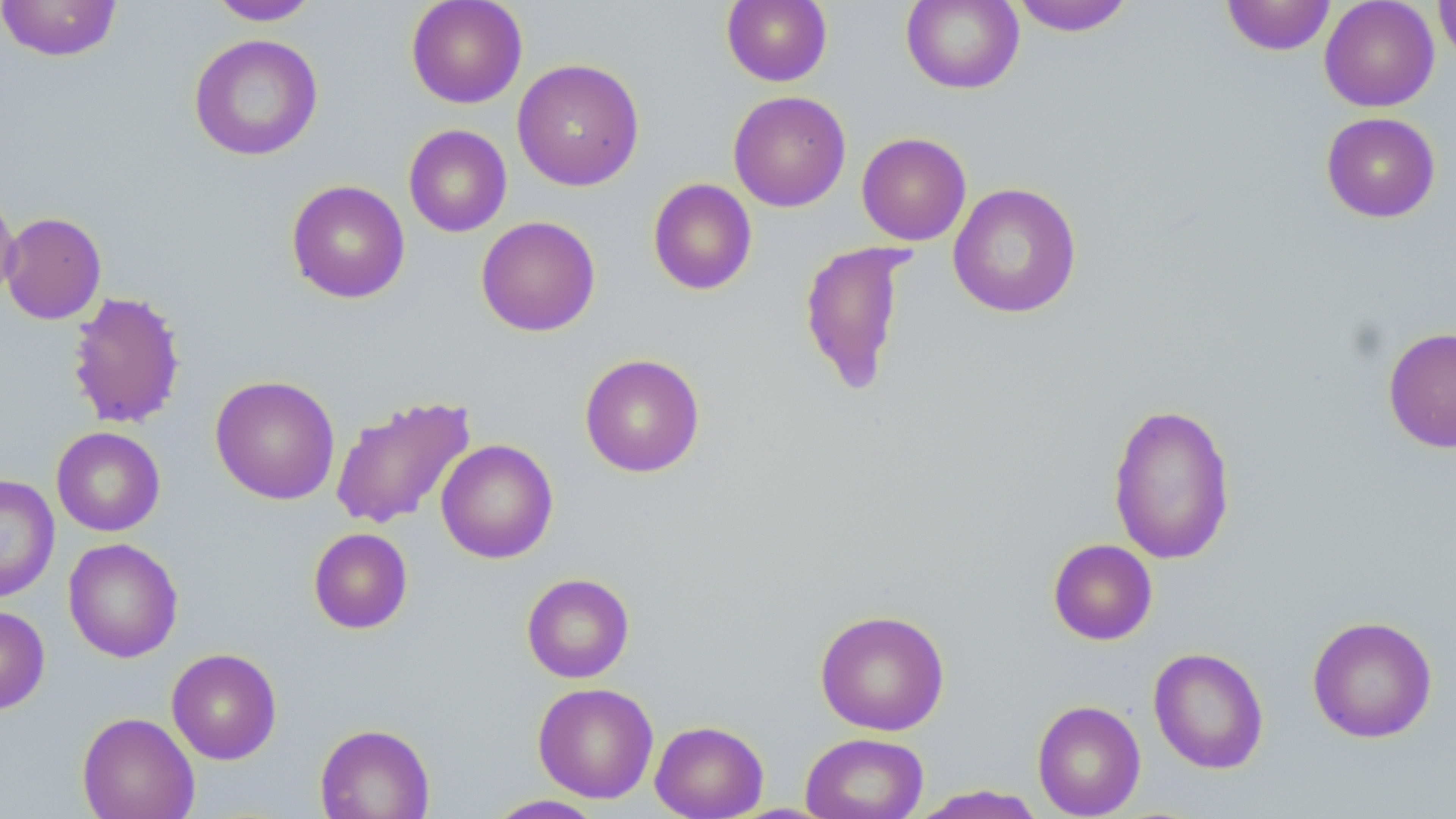 Approximate bounding boxes as named x1/y1/x2/y2 corners in pixels. Uninfected red blood cell locations: (x1=0, y1=0, x2=122, y2=61), (x1=406, y1=0, x2=528, y2=108), (x1=721, y1=0, x2=832, y2=87), (x1=1221, y1=0, x2=1336, y2=55), (x1=1319, y1=0, x2=1439, y2=112), (x1=1434, y1=0, x2=1456, y2=66), (x1=206, y1=1, x2=321, y2=25), (x1=901, y1=1, x2=1024, y2=94), (x1=1009, y1=1, x2=1136, y2=36), (x1=188, y1=33, x2=323, y2=162), (x1=512, y1=58, x2=645, y2=191), (x1=728, y1=90, x2=851, y2=212), (x1=1321, y1=112, x2=1440, y2=222), (x1=403, y1=124, x2=512, y2=237), (x1=856, y1=132, x2=971, y2=245), (x1=647, y1=178, x2=758, y2=296), (x1=0, y1=179, x2=20, y2=308), (x1=286, y1=179, x2=410, y2=304), (x1=948, y1=183, x2=1083, y2=318), (x1=1, y1=212, x2=107, y2=324), (x1=476, y1=215, x2=601, y2=337), (x1=798, y1=240, x2=916, y2=397), (x1=66, y1=290, x2=186, y2=430), (x1=1382, y1=326, x2=1456, y2=452), (x1=579, y1=353, x2=705, y2=478), (x1=210, y1=375, x2=340, y2=505), (x1=329, y1=394, x2=477, y2=531), (x1=1107, y1=402, x2=1236, y2=565), (x1=51, y1=426, x2=165, y2=536), (x1=436, y1=439, x2=558, y2=564), (x1=0, y1=475, x2=59, y2=602), (x1=308, y1=527, x2=413, y2=633), (x1=63, y1=538, x2=182, y2=663), (x1=1048, y1=539, x2=1158, y2=645), (x1=521, y1=573, x2=635, y2=683), (x1=0, y1=605, x2=50, y2=714), (x1=814, y1=609, x2=950, y2=736), (x1=1307, y1=615, x2=1438, y2=743), (x1=1148, y1=647, x2=1269, y2=774), (x1=166, y1=648, x2=282, y2=765), (x1=532, y1=682, x2=658, y2=803), (x1=1032, y1=700, x2=1146, y2=818), (x1=77, y1=712, x2=199, y2=819), (x1=650, y1=720, x2=769, y2=819), (x1=314, y1=722, x2=435, y2=818), (x1=800, y1=732, x2=929, y2=819), (x1=910, y1=785, x2=1048, y2=818), (x1=484, y1=794, x2=608, y2=818). Slide-level diagnosis: no evidence of blood parasites. Light microscopy. May-Grünwald-Giemsa stain. Thin blood smear. One field of a larger specimen. Image is 1456×819 pixels. 1000x magnification.